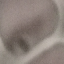
{
  "malaria_status": "uninfected",
  "stain": "Giemsa",
  "capture": "smartphone camera at the microscope eyepiece",
  "preparation": "thin smear",
  "image_type": "cell patch, automatically extracted from a larger field of view and resized to 64 × 64 pixels"
}